Point out each Plasmodium parasite.
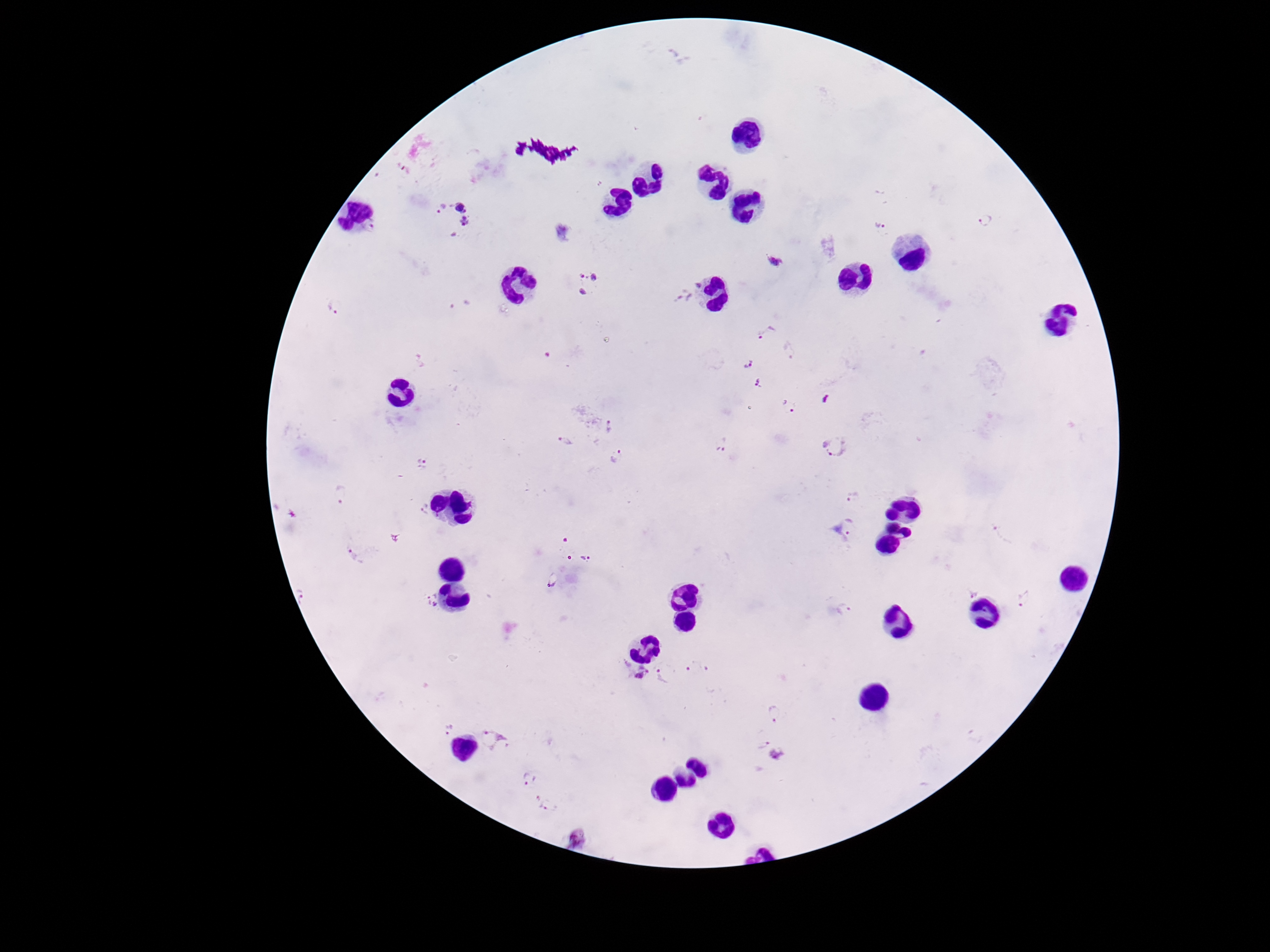

Approximate centers as {x, y} in pixels.
Plasmodium parasites: {402, 169}, {451, 216}, {984, 220}, {879, 224}, {774, 263}, {588, 283}, {682, 298}, {332, 306}, {458, 307}, {766, 332}, {788, 351}, {747, 363}, {758, 384}, {790, 407}, {613, 427}, {566, 442}, {721, 445}, {835, 447}, {615, 456}, {420, 464}, {854, 496}, {423, 511}, {850, 528}, {1003, 535}, {565, 539}, {357, 555}, {585, 558}, {553, 580}, {972, 591}, {1026, 598}, {431, 600}, {847, 610}, {696, 667}, {639, 671}, {664, 674}, {774, 714}, {452, 727}, {498, 738}, {761, 744}, {778, 754}, {529, 778}, {545, 804}, {575, 840}.

Smartphone photograph taken through the microscope eyepiece. One field from this slide. Image is 1270×952 pixels. Thick blood film. Patient malaria status: positive. Giemsa stain. 100x magnification.